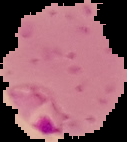

{
  "malaria_status": "parasitized",
  "preparation": "thin blood smear",
  "image_size": "127×142 pixels",
  "image_type": "segmented cell region with the area outside set to black"
}